State which cell type is depicted.
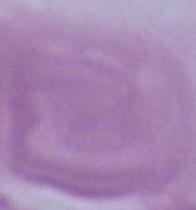

An erythrocyte.

Photomicrograph. Captured at 1000x magnification.